Report the malaria status of this cell.
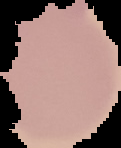
Uninfected.

From a thin blood smear. Image is 121×148 pixels. The area outside the segmented cell region is set to black.